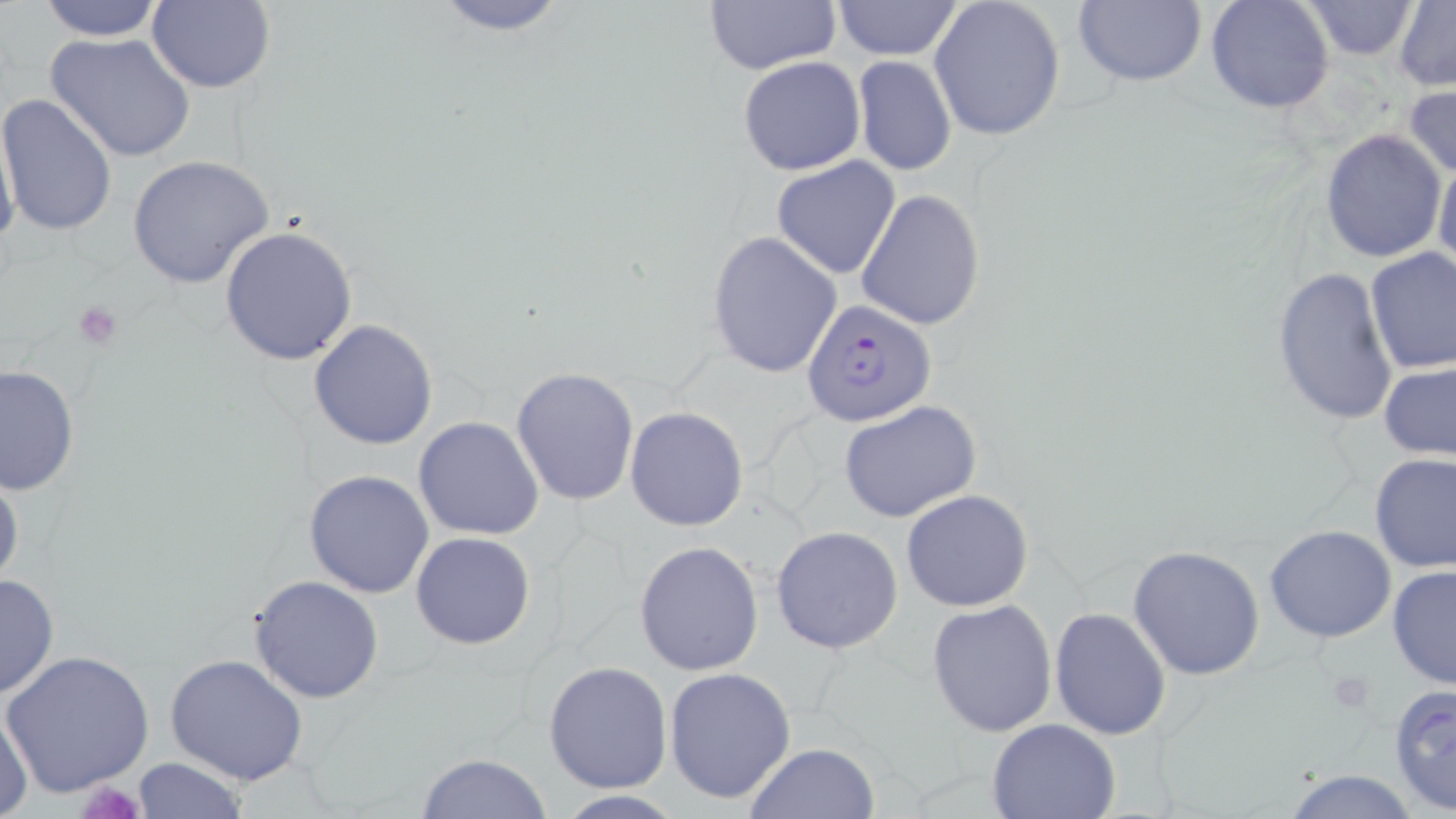

{
  "slide_level_diagnosis": "Plasmodium falciparum",
  "magnification": "1000x",
  "platelet_locations": "approximate bounding boxes as [x1, y1, x2, y2] in pixels: [73, 301, 124, 350], [73, 781, 149, 819]",
  "uninfected_red_blood_cell_locations": "approximate bounding boxes as [x1, y1, x2, y2] in pixels: [35, 0, 169, 41], [427, 0, 574, 36], [928, 0, 1066, 142], [1073, 0, 1207, 88], [1204, 0, 1334, 115], [1300, 0, 1420, 60], [146, 1, 276, 94], [704, 1, 837, 74], [830, 1, 965, 60], [1395, 1, 1455, 90], [46, 33, 195, 162], [738, 56, 865, 176], [853, 56, 956, 176], [1404, 81, 1456, 183], [0, 93, 119, 236], [0, 108, 22, 260], [1319, 129, 1447, 263], [1434, 149, 1456, 283], [129, 155, 276, 290], [771, 157, 901, 280], [855, 188, 986, 331], [220, 226, 360, 366], [706, 232, 841, 378], [1364, 247, 1455, 374], [1271, 265, 1400, 428], [309, 319, 439, 450], [1380, 363, 1456, 461], [0, 364, 79, 498], [511, 367, 641, 507], [839, 399, 982, 523], [625, 407, 749, 531], [414, 416, 545, 539], [1369, 452, 1455, 572], [0, 462, 24, 593], [304, 470, 434, 597], [900, 489, 1034, 612], [770, 525, 905, 654], [1265, 525, 1396, 643], [409, 530, 536, 651], [634, 540, 763, 675], [1127, 546, 1265, 681], [1387, 563, 1456, 692], [0, 573, 59, 700], [247, 575, 384, 703], [927, 600, 1058, 738], [1048, 607, 1172, 740], [4, 650, 157, 797], [165, 654, 309, 787], [543, 660, 672, 792], [664, 666, 796, 805], [1388, 683, 1456, 816], [0, 700, 33, 818], [986, 718, 1121, 819], [743, 743, 879, 819], [416, 751, 555, 819], [131, 758, 248, 817], [1277, 767, 1425, 819]",
  "modality": "light microscopy",
  "plasmodium_falciparum_infected_red_blood_cell_locations": "approximate bounding boxes as [x1, y1, x2, y2] in pixels: [803, 297, 935, 427]",
  "field_of_view": "single",
  "preparation": "thin blood film",
  "image_size": "1456×819 pixels",
  "stain": "May-Grünwald-Giemsa"
}